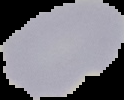

Segmented cell region on a black background. Image is 124×100 pixels. Result: no malaria parasites detected. From a thin blood smear.